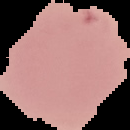 Image is 130×130 pixels. Malaria status: uninfected. Cell region segmented out of the field of view; the surrounding area is masked to black. From a thin blood film.